Assess this cell for malaria.
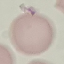

It is uninfected.

{
  "capture": "smartphone through the microscope eyepiece",
  "preparation": "thin blood smear",
  "image_type": "cell patch, automatically extracted from a larger field of view and resized to 64 × 64 pixels",
  "stain": "Giemsa"
}